Point out every malaria parasite and every leukocyte.
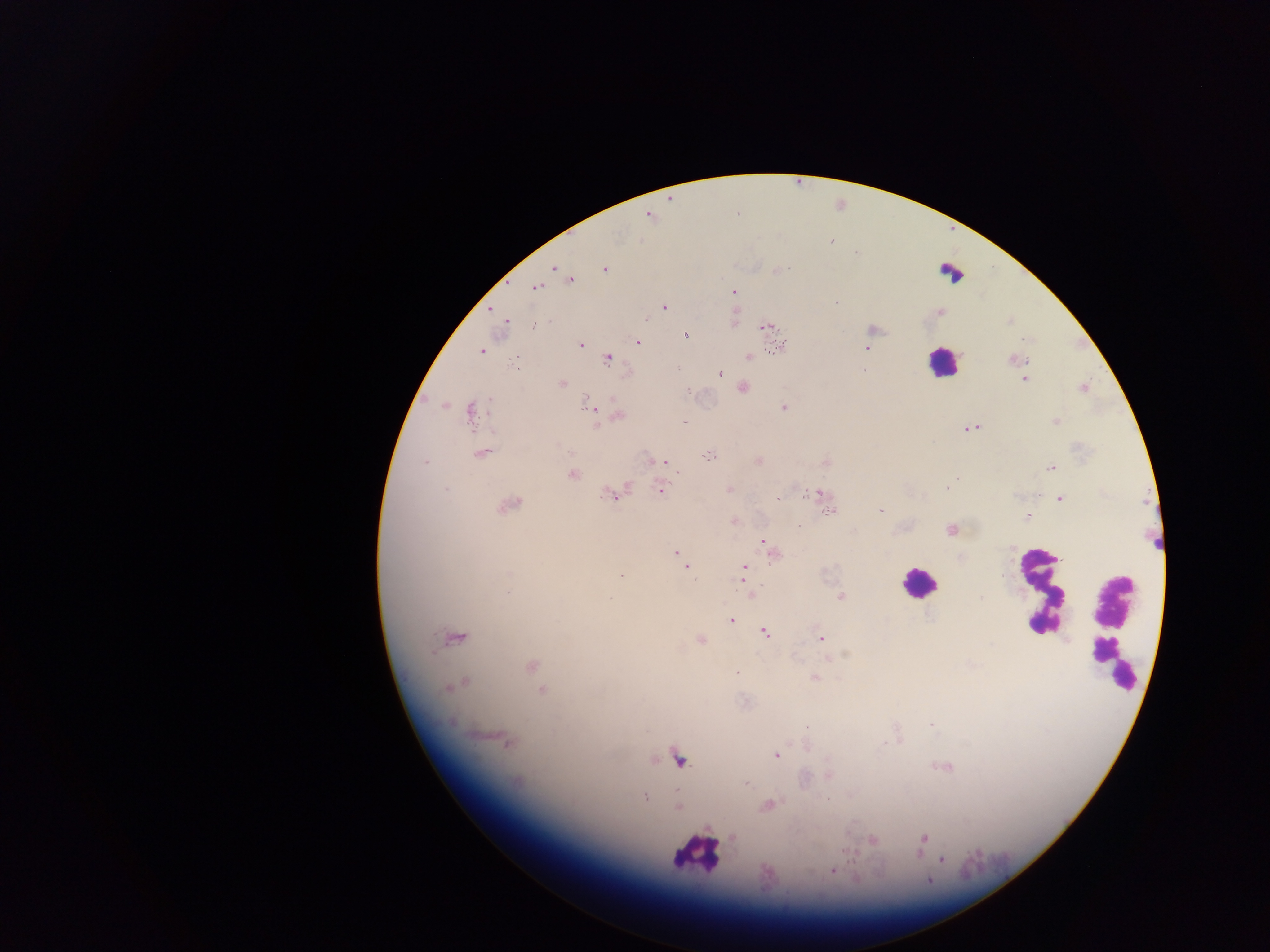
Approximate centers as (x, y) in pixels.
Malaria parasites: (646, 215), (829, 244), (553, 267), (605, 268), (779, 270), (570, 280), (535, 288), (734, 290), (664, 307), (490, 310), (941, 311), (644, 320), (506, 322), (764, 327), (872, 330), (686, 335), (639, 343), (581, 344), (779, 345), (866, 347), (481, 351), (749, 357), (608, 358), (1020, 358), (677, 368), (720, 375), (1026, 379), (561, 384), (744, 387), (1082, 388), (584, 396), (612, 399), (784, 407), (469, 414), (618, 416), (1055, 422), (597, 424), (973, 427), (964, 430), (707, 454), (480, 455), (656, 460), (665, 461), (424, 462), (758, 462), (1052, 467), (570, 474), (946, 487), (446, 488), (660, 488), (727, 488), (818, 493), (609, 495), (618, 495), (777, 497), (1060, 498), (507, 506), (880, 510), (829, 512), (1026, 515), (734, 520), (950, 529), (763, 542), (675, 551), (687, 567), (744, 567), (690, 572), (622, 576), (745, 586), (840, 597), (980, 598), (731, 621), (765, 634), (821, 638), (454, 639), (701, 640), (1067, 640), (845, 653), (530, 666), (814, 677), (465, 681), (448, 688), (541, 690), (930, 725), (505, 742), (885, 744), (775, 755), (677, 759), (945, 766), (829, 776), (748, 785), (827, 796), (645, 797), (768, 805), (677, 807), (924, 839), (871, 841), (941, 861), (832, 869), (930, 882).
Leukocytes: (941, 363), (914, 583).

image_size: 1270×952 pixels
field_of_view: single
capture: mobile-phone photograph through a microscope
preparation: thick blood film
country: Ghana